Describe the morphology of the red blood cells.
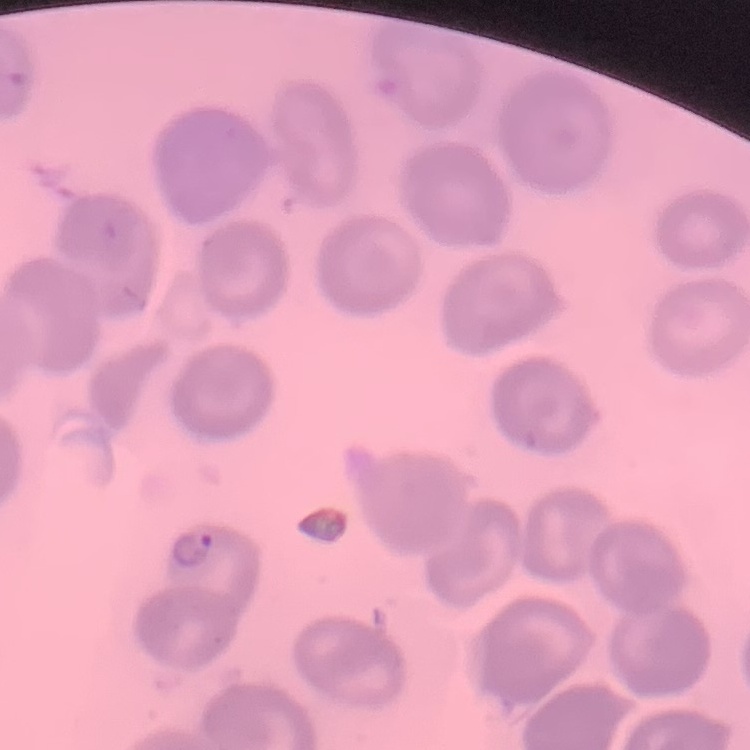
No rouleaux formation.

Thin peripheral smear. Field's or Giemsa stain. Square crop of a larger photomicrograph.